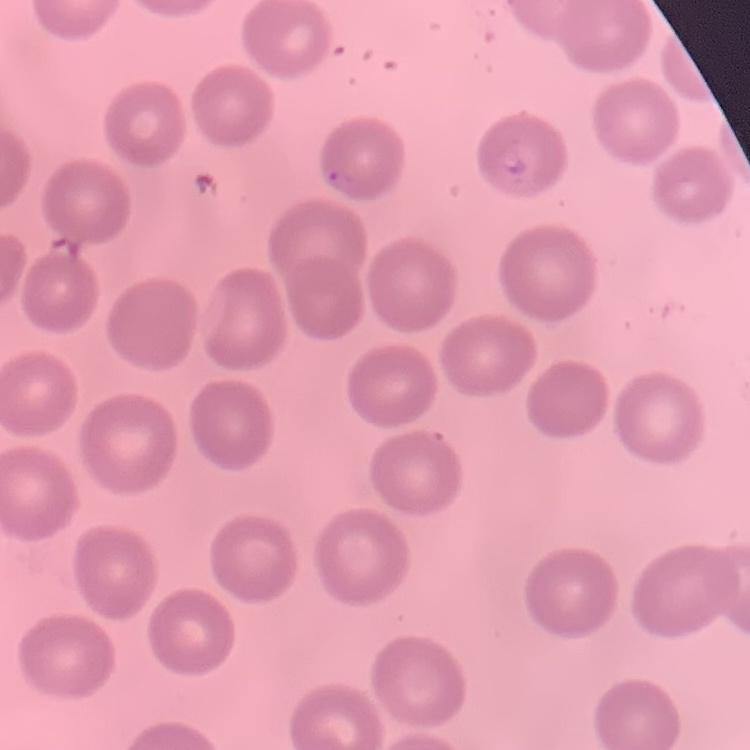 The erythrocytes exhibit no rouleaux formation. Stained with either Field's or Giemsa. Square crop of a larger photomicrograph. Thin blood film.